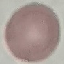 Malaria status: uninfected. Cell patch, automatically extracted from a larger field of view and resized to 64 × 64 pixels. Acquired by smartphone through the microscope eyepiece. Thin blood film. Giemsa stain.